Locate every leukocyte (white blood cell).
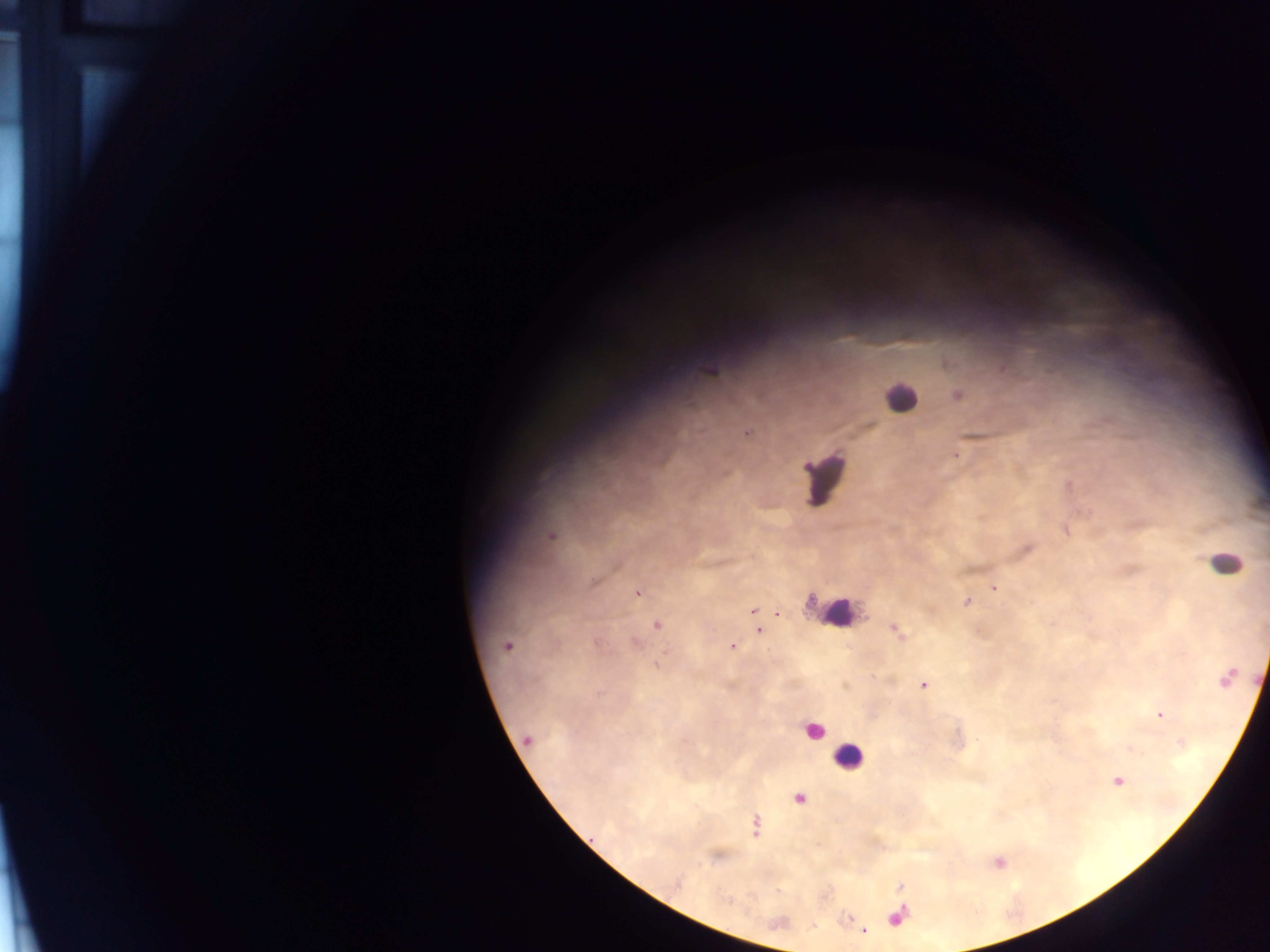
Approximate centers as x y in pixels.
Leukocytes: 902 398; 1218 558; 841 615; 845 757.

capture = mobile-phone photograph through a microscope
Plasmodium parasite locations = approximate centers as x y in pixels: 958 455; 994 586; 636 593; 753 610; 774 613; 759 631; 732 645; 924 685; 1159 715; 862 932
image size = 1270×952 pixels
field of view = single
country = Ghana
preparation = thick blood film